Locate and identify every blood parasite.
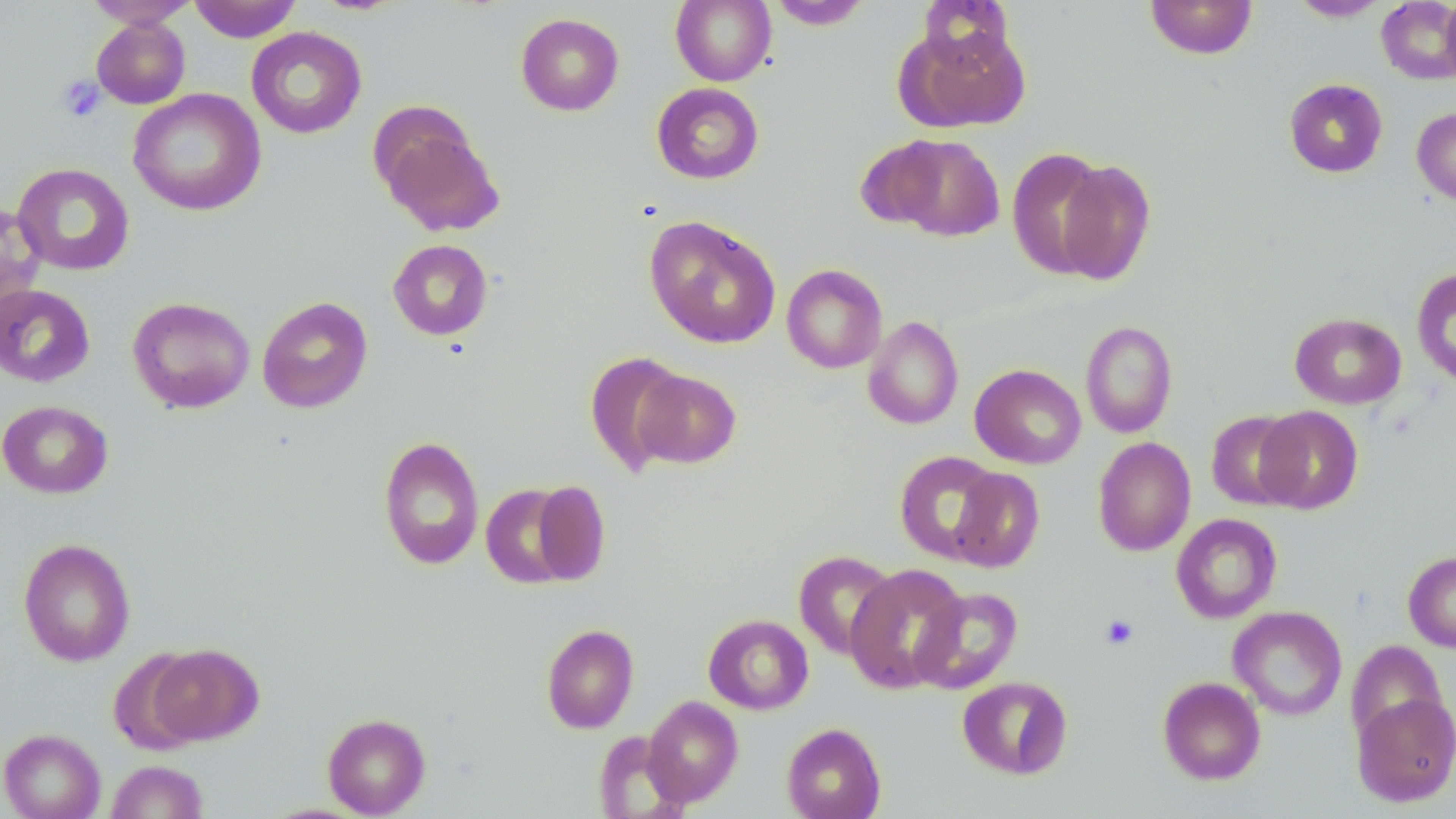

No blood parasites seen.

slide-level diagnosis = negative for blood parasites
platelet locations = approximate bounding boxes as (x1,y1)-(x2,y2) corner pairs in pixels: (57,75)-(106,122), (1100,615)-(1139,650)
field of view = one of a larger specimen
uninfected red blood cell locations = approximate bounding boxes as (x1,y1)-(x2,y2) corner pairs in pixels: (83,0)-(199,28), (189,0)-(303,43), (670,0)-(776,86), (917,0)-(1016,72), (1144,0)-(1259,59), (1288,0)-(1390,21), (1440,0)-(1456,87), (766,1)-(873,30), (1376,1)-(1456,85), (515,13)-(624,116), (91,16)-(191,109), (899,25)-(1031,133), (246,27)-(367,139), (1284,78)-(1388,178), (651,82)-(764,184), (128,88)-(266,216), (1412,107)-(1456,207), (373,113)-(505,238), (890,134)-(1005,241), (854,137)-(951,231), (1007,147)-(1112,280), (1051,158)-(1156,286), (12,163)-(135,276), (0,200)-(45,314), (644,215)-(781,349), (388,239)-(493,341), (782,264)-(888,373), (1412,265)-(1456,391), (0,284)-(95,388), (257,296)-(373,414), (127,297)-(255,413), (1289,312)-(1406,409), (863,316)-(963,430), (1080,320)-(1178,438), (584,351)-(689,477), (970,364)-(1086,469), (632,368)-(742,469), (0,400)-(113,499), (1254,405)-(1364,514), (1205,410)-(1305,510), (378,436)-(484,571), (1093,437)-(1196,556), (894,451)-(1003,563), (948,467)-(1045,572), (529,480)-(611,584), (480,483)-(581,589), (1171,513)-(1282,623), (18,538)-(136,667), (793,550)-(899,660), (1403,551)-(1456,652), (844,563)-(968,693), (911,587)-(1023,694), (1228,605)-(1348,721), (703,614)-(814,715), (541,624)-(639,734), (1345,640)-(1447,747), (147,644)-(263,746), (108,649)-(208,756), (957,675)-(1073,780), (1158,676)-(1266,785), (1352,691)-(1456,806), (642,695)-(743,808), (322,712)-(431,817), (781,723)-(886,819), (0,728)-(105,819), (592,731)-(691,818), (105,759)-(208,819)
modality = optical microscopy
stain = May-Grünwald-Giemsa
image size = 1456×819 pixels
preparation = thin blood film
magnification = 1000x